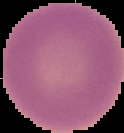

Summary:
  - Image size: 124×133 pixels
  - Image type: cell region segmented out of the field of view; surrounding area masked to black
  - Malaria status: uninfected
  - Preparation: thin blood film